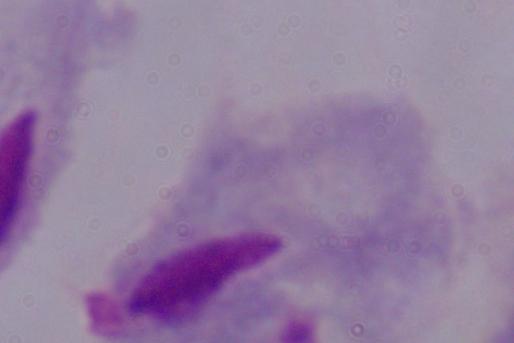

Captured at 1000x magnification. Photomicrograph. A trichomonad is seen.